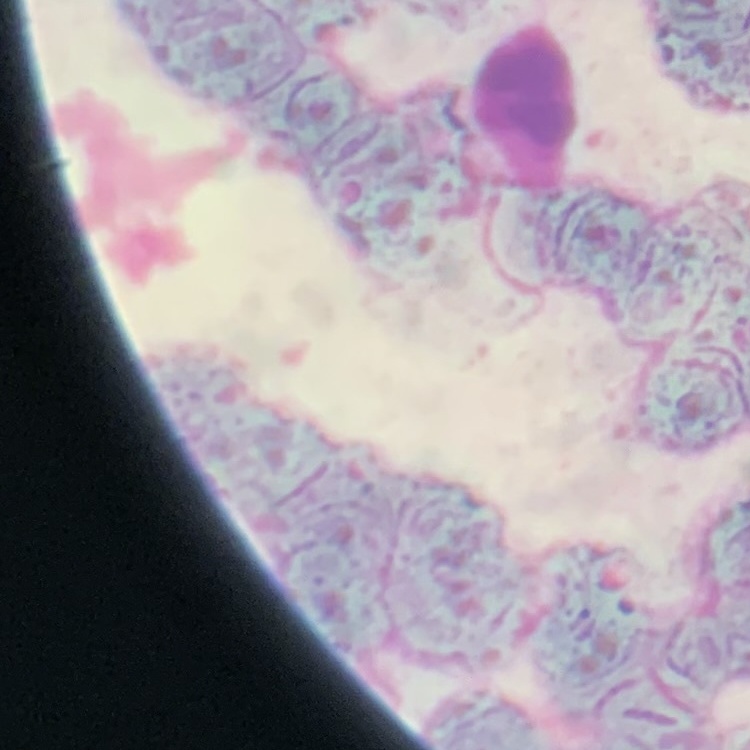

erythrocyte_morphology: rouleaux formation
stain: Field's or Giemsa
preparation: thin blood film
image_type: one tile cut from a larger photomicrograph